Report the malaria status of this cell.
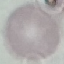

It is uninfected.

Summary:
  - Preparation: thin blood film
  - Stain: Giemsa
  - Capture: smartphone camera at the microscope eyepiece
  - Image type: cell patch, automatically extracted from a larger field of view and resized to 64 × 64 pixels